Assess the morphology of the red blood cells.
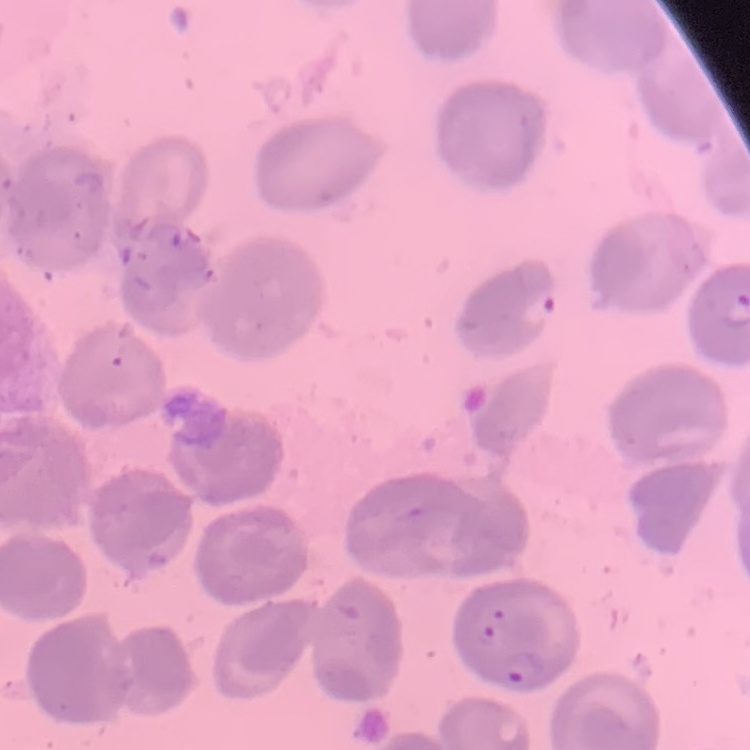
No rouleaux formation.

preparation: thin blood film
image_type: square crop of a larger photomicrograph
stain: Field's or Giemsa